Classify this cell by malaria status.
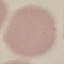
It is uninfected.

Giemsa-stained preparation. Automatically extracted cell patch, resized to 64 × 64 pixels. Photographed with a smartphone camera at the microscope eyepiece. Thin smear of blood.